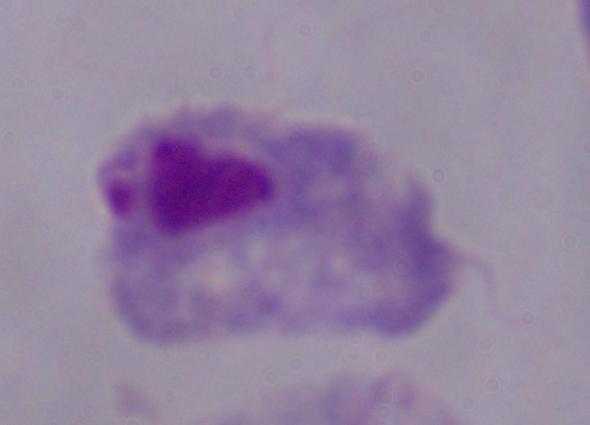

Photomicrograph. A trichomonad is seen. Captured at 1000x magnification.